State the blood parasite species.
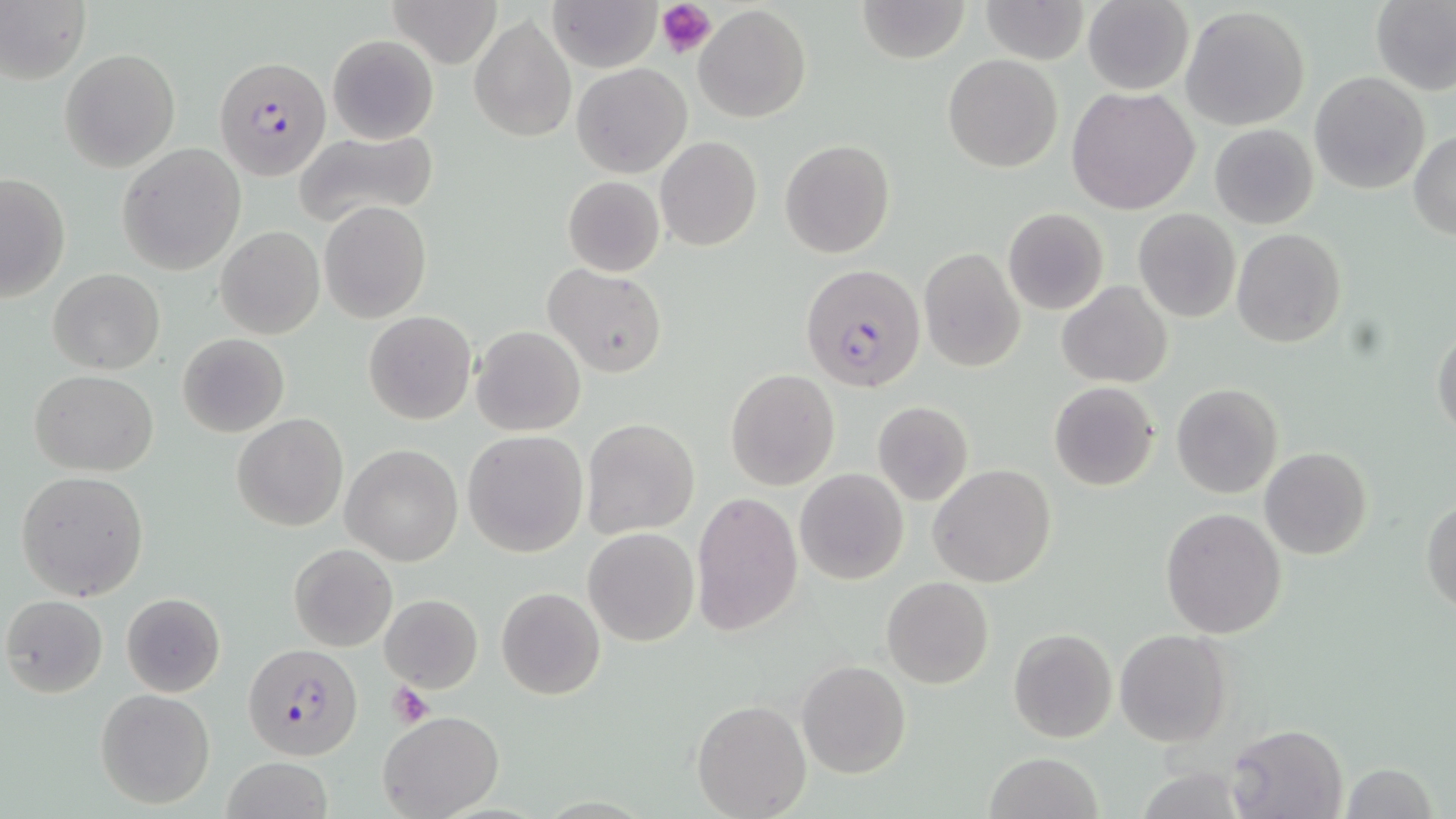

Plasmodium falciparum.

Approximate bounding boxes as (x1, y1, x2, y2) in pixels. Plasmodium falciparum-infected red blood cell locations: (212, 55, 329, 178), (800, 263, 925, 394), (244, 641, 362, 760). Uninfected red blood cell locations: (0, 0, 89, 83), (386, 0, 504, 68), (547, 0, 662, 71), (857, 0, 970, 64), (1081, 0, 1195, 94), (1371, 0, 1456, 95), (982, 1, 1088, 63), (695, 4, 811, 125), (1181, 7, 1311, 131), (470, 14, 575, 143), (326, 33, 440, 145), (59, 48, 180, 171), (942, 54, 1064, 172), (572, 63, 692, 177), (1308, 72, 1431, 193), (1066, 85, 1201, 215), (1208, 124, 1319, 229), (293, 127, 439, 228), (1411, 128, 1456, 238), (655, 136, 762, 250), (780, 139, 895, 258), (116, 144, 247, 275), (0, 172, 71, 303), (563, 175, 665, 277), (318, 200, 432, 323), (1003, 208, 1110, 314), (1133, 208, 1240, 322), (216, 226, 325, 340), (1231, 228, 1346, 347), (919, 249, 1025, 371), (544, 265, 668, 378), (48, 268, 165, 375), (1058, 281, 1172, 387), (363, 312, 477, 425), (1430, 323, 1455, 440), (471, 325, 586, 437), (176, 333, 289, 438), (725, 368, 840, 491), (30, 370, 159, 476), (1049, 381, 1160, 491), (1171, 384, 1283, 498), (872, 401, 974, 506), (232, 413, 348, 531), (581, 419, 700, 538), (463, 430, 588, 557), (341, 445, 463, 565), (1260, 448, 1371, 560), (929, 464, 1056, 587), (795, 468, 909, 584), (16, 471, 149, 602), (691, 491, 805, 637), (1422, 500, 1456, 614), (1160, 508, 1287, 639), (583, 528, 700, 647), (288, 543, 397, 652), (882, 577, 995, 689), (497, 587, 605, 699), (120, 592, 226, 698), (379, 594, 483, 693), (3, 595, 108, 697), (1008, 629, 1117, 743), (1115, 629, 1233, 747), (797, 660, 911, 779), (95, 689, 214, 808), (692, 699, 811, 817), (377, 710, 504, 819), (1227, 723, 1347, 818), (983, 753, 1102, 819), (220, 758, 332, 819), (1341, 762, 1438, 818). Platelet locations: (658, 0, 716, 57), (386, 683, 435, 727). Thin blood film. May-Grünwald-Giemsa-stained preparation. Single field of view. Image is 1456×819 pixels. 1000x magnification. Light microscopy.